Give the extent of all uninfected red blood cells.
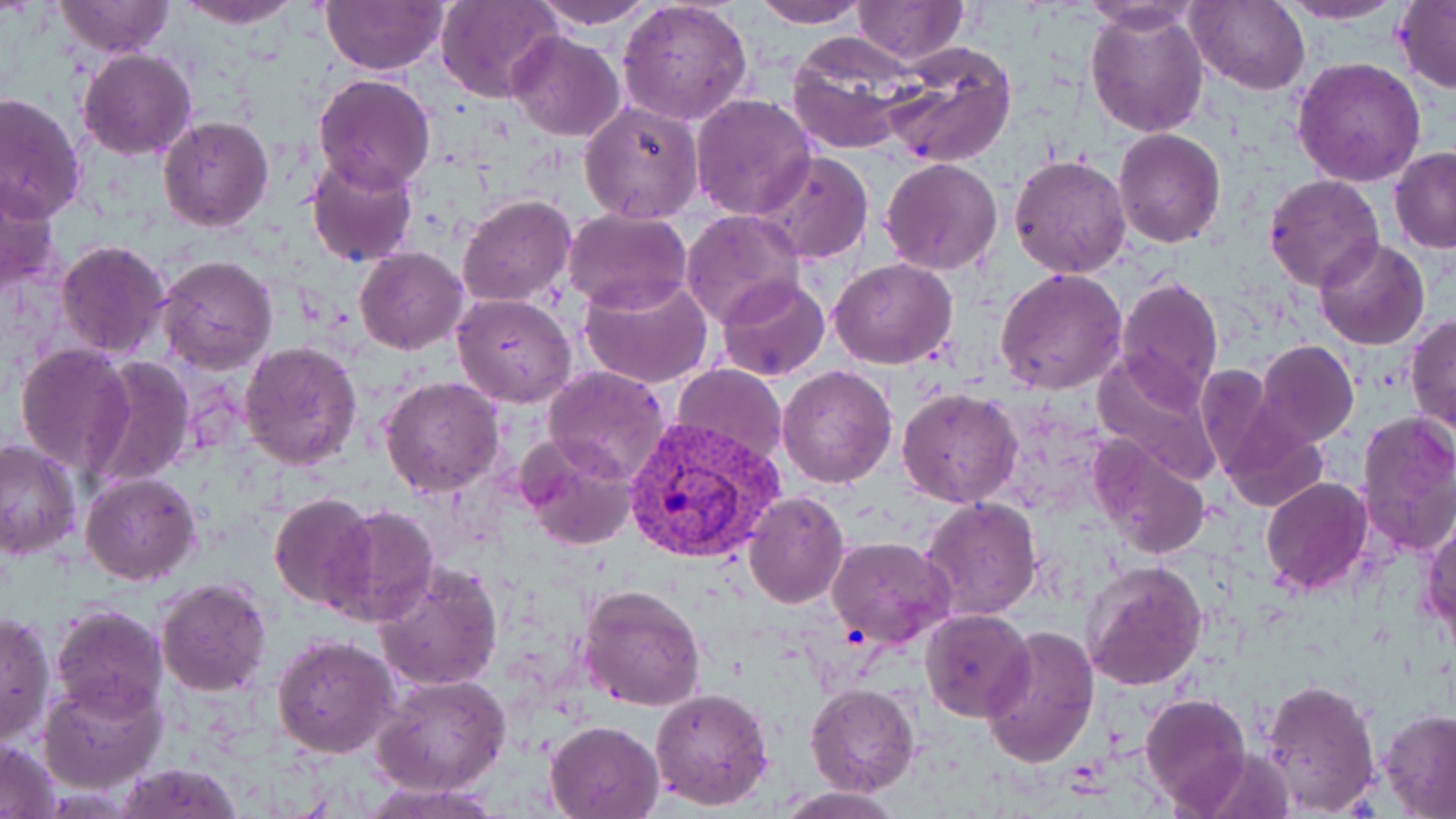
Approximate bounding boxes as named x1/y1/x2/y2 corners in pixels.
Uninfected red blood cells: (x1=176, y1=0, x2=304, y2=27), (x1=529, y1=0, x2=658, y2=29), (x1=617, y1=0, x2=753, y2=123), (x1=852, y1=0, x2=966, y2=64), (x1=1277, y1=0, x2=1405, y2=24), (x1=55, y1=1, x2=174, y2=59), (x1=321, y1=1, x2=448, y2=74), (x1=750, y1=1, x2=869, y2=27), (x1=1188, y1=1, x2=1310, y2=95), (x1=1392, y1=1, x2=1456, y2=94), (x1=434, y1=2, x2=562, y2=103), (x1=1079, y1=3, x2=1204, y2=33), (x1=1086, y1=6, x2=1209, y2=138), (x1=506, y1=31, x2=625, y2=140), (x1=785, y1=34, x2=915, y2=155), (x1=878, y1=41, x2=1017, y2=169), (x1=79, y1=49, x2=197, y2=161), (x1=1293, y1=57, x2=1427, y2=188), (x1=312, y1=71, x2=436, y2=192), (x1=0, y1=92, x2=86, y2=222), (x1=691, y1=94, x2=816, y2=222), (x1=579, y1=100, x2=705, y2=224), (x1=158, y1=116, x2=273, y2=232), (x1=1114, y1=129, x2=1225, y2=247), (x1=1390, y1=147, x2=1456, y2=252), (x1=752, y1=151, x2=874, y2=263), (x1=1009, y1=153, x2=1131, y2=280), (x1=307, y1=154, x2=419, y2=268), (x1=880, y1=157, x2=1002, y2=276), (x1=1263, y1=174, x2=1384, y2=292), (x1=0, y1=177, x2=63, y2=292), (x1=458, y1=194, x2=576, y2=308), (x1=563, y1=207, x2=692, y2=314), (x1=681, y1=209, x2=803, y2=327), (x1=1314, y1=237, x2=1430, y2=350), (x1=54, y1=239, x2=172, y2=360), (x1=354, y1=247, x2=468, y2=355), (x1=156, y1=254, x2=278, y2=375), (x1=830, y1=258, x2=957, y2=369), (x1=996, y1=267, x2=1128, y2=395), (x1=579, y1=275, x2=715, y2=387), (x1=1116, y1=275, x2=1224, y2=409), (x1=716, y1=277, x2=831, y2=383), (x1=451, y1=292, x2=577, y2=407), (x1=1407, y1=313, x2=1456, y2=437), (x1=1256, y1=340, x2=1359, y2=445), (x1=14, y1=341, x2=132, y2=474), (x1=241, y1=341, x2=363, y2=468), (x1=1089, y1=355, x2=1223, y2=485), (x1=84, y1=356, x2=197, y2=489), (x1=1193, y1=362, x2=1286, y2=480), (x1=672, y1=363, x2=789, y2=463), (x1=542, y1=364, x2=670, y2=485), (x1=778, y1=365, x2=897, y2=488), (x1=380, y1=376, x2=504, y2=498), (x1=897, y1=388, x2=1023, y2=509), (x1=1355, y1=411, x2=1456, y2=557), (x1=1220, y1=416, x2=1329, y2=512), (x1=516, y1=437, x2=639, y2=551), (x1=1089, y1=437, x2=1211, y2=560), (x1=0, y1=439, x2=82, y2=561), (x1=81, y1=471, x2=201, y2=586), (x1=1260, y1=476, x2=1373, y2=594), (x1=743, y1=491, x2=848, y2=609), (x1=268, y1=493, x2=376, y2=611), (x1=920, y1=497, x2=1040, y2=620), (x1=327, y1=504, x2=437, y2=628), (x1=1421, y1=518, x2=1454, y2=650), (x1=827, y1=536, x2=956, y2=649), (x1=374, y1=562, x2=503, y2=692), (x1=1082, y1=562, x2=1209, y2=690), (x1=156, y1=576, x2=271, y2=697), (x1=578, y1=582, x2=708, y2=713), (x1=51, y1=604, x2=168, y2=718), (x1=919, y1=609, x2=1034, y2=722), (x1=1, y1=611, x2=54, y2=747), (x1=980, y1=625, x2=1099, y2=769), (x1=272, y1=634, x2=400, y2=756), (x1=373, y1=674, x2=510, y2=794), (x1=38, y1=677, x2=167, y2=795), (x1=1261, y1=678, x2=1381, y2=813), (x1=805, y1=683, x2=920, y2=797), (x1=650, y1=686, x2=774, y2=811), (x1=1139, y1=693, x2=1250, y2=814), (x1=1378, y1=709, x2=1456, y2=816), (x1=545, y1=720, x2=665, y2=817), (x1=1, y1=738, x2=60, y2=817), (x1=111, y1=763, x2=244, y2=818), (x1=363, y1=780, x2=496, y2=818), (x1=776, y1=787, x2=904, y2=818).

Plasmodium vivax-infected red blood cell locations: (x1=620, y1=416, x2=785, y2=566). Slide-level diagnosis: Plasmodium vivax. Optical microscopy. Thin blood smear. May-Grünwald-Giemsa-stained preparation. Image is 1456×819 pixels. Captured at 1000x magnification. One field of a larger specimen.